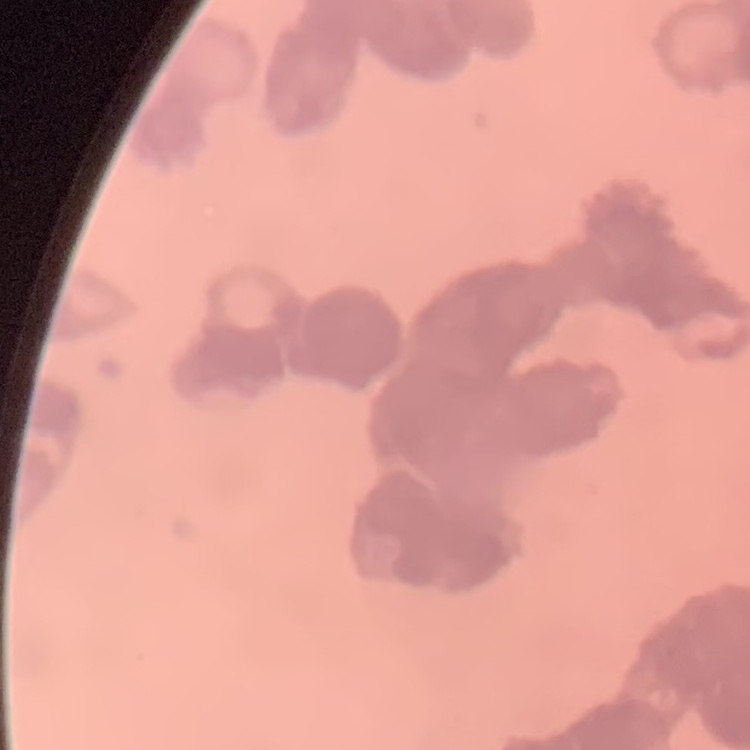
red blood cell morphology = rouleaux formation
preparation = thin peripheral smear
stain = Field's or Giemsa
image type = square crop of a larger photomicrograph